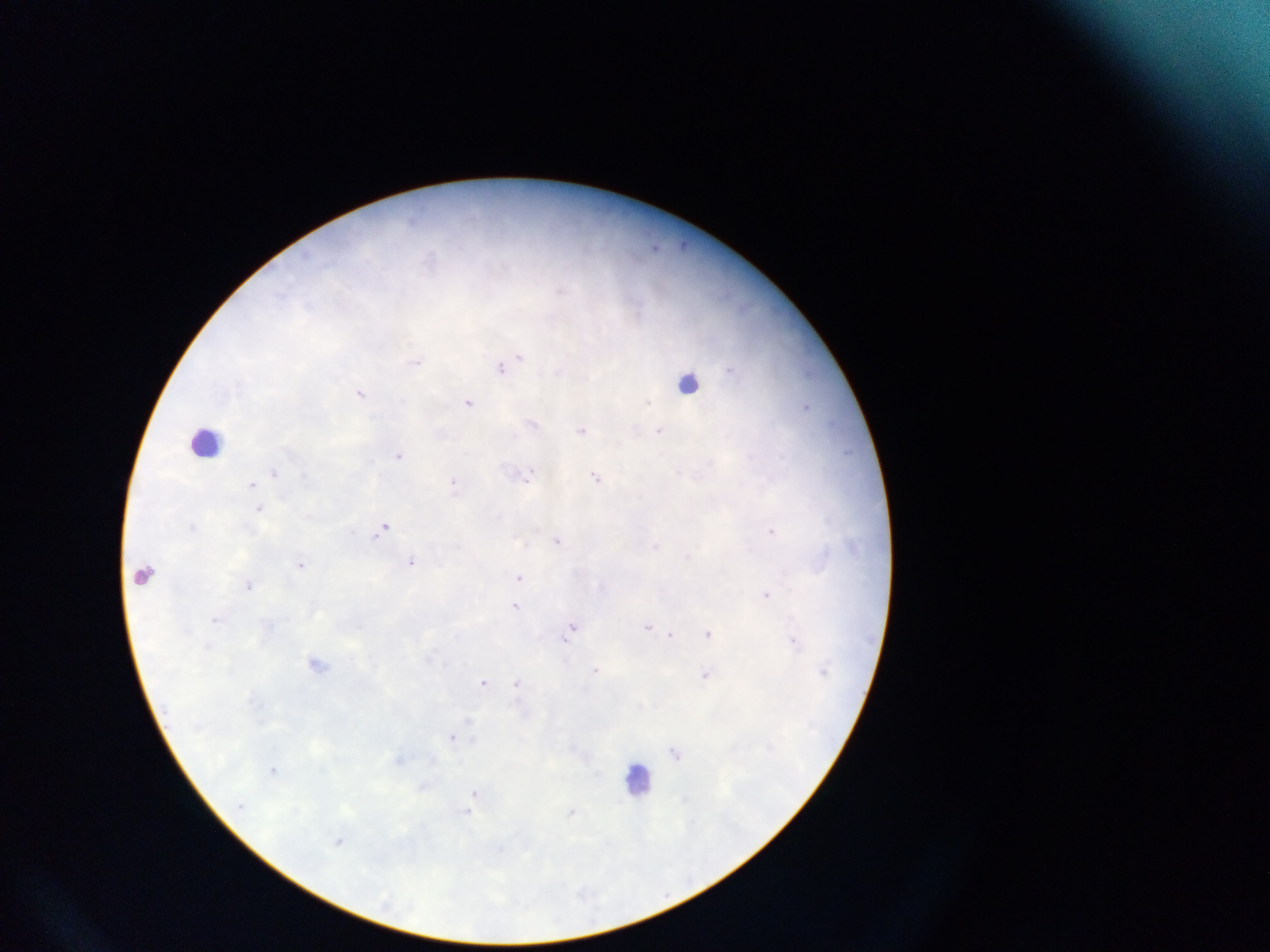
preparation = thick blood film
image size = 1270×952 pixels
leukocyte locations = approximate centers as (x, y) in pixels: (687, 383), (206, 442), (145, 574), (638, 778)
capture = mobile-phone photograph through a microscope
Plasmodium parasite locations = approximate centers as (x, y) in pixels: (413, 219), (683, 246), (656, 248), (519, 355), (416, 361), (501, 367), (558, 372), (361, 393), (468, 402), (649, 403), (807, 406), (533, 423), (582, 430), (659, 431), (399, 454), (274, 472), (679, 473), (529, 476), (596, 477), (454, 483), (252, 484), (259, 509), (499, 516), (192, 526), (384, 527), (771, 530), (557, 540), (655, 545), (689, 557), (412, 562), (300, 564), (519, 576), (248, 584), (767, 594), (515, 606), (215, 619), (572, 627), (648, 627), (708, 632), (568, 634), (671, 634), (794, 640), (318, 663), (595, 669), (705, 674), (483, 681), (516, 682), (468, 720), (452, 736), (472, 741), (675, 753), (400, 758), (273, 770), (474, 794), (469, 809), (571, 812), (339, 840)
field of view = single
country = Ghana